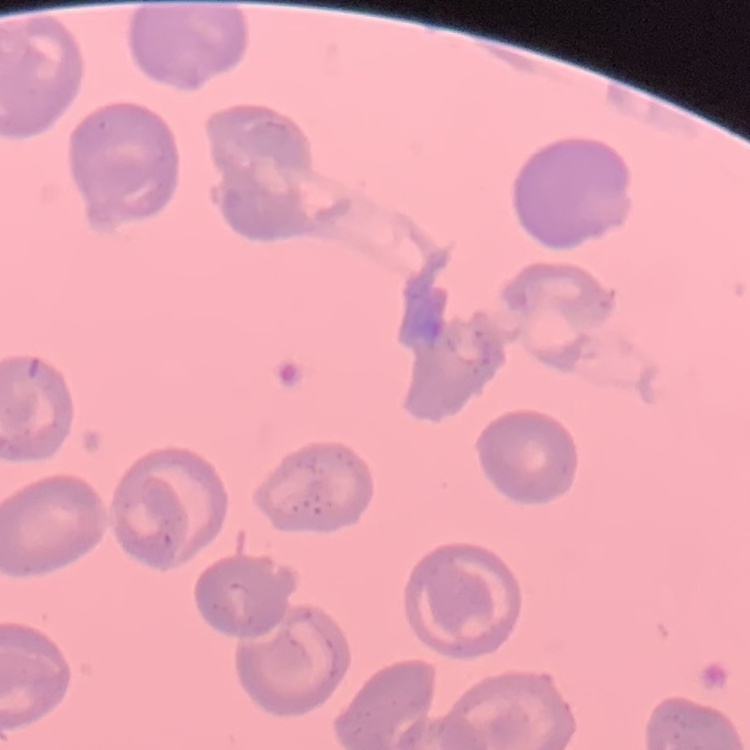
erythrocyte morphology = no rouleaux formation
stain = Field's or Giemsa
image type = one tile cut from a larger photomicrograph
preparation = thin blood film